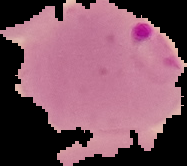

{
  "image_type": "cell region segmented out of the field of view; surrounding area masked to black",
  "malaria_status": "parasitized",
  "preparation": "thin blood smear",
  "image_size": "187×166 pixels"
}